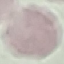
Result: negative for malaria parasites. Automatically extracted cell patch, resized to 64 × 64 pixels. Giemsa-stained preparation. Acquired by smartphone through the microscope eyepiece. Thin blood film.